Identify the parasite.
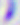
Toxoplasma gondii.

Micrograph. 400x magnification.